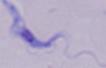

{
  "identification": "trypanosome",
  "magnification": "1000x",
  "modality": "micrograph"
}